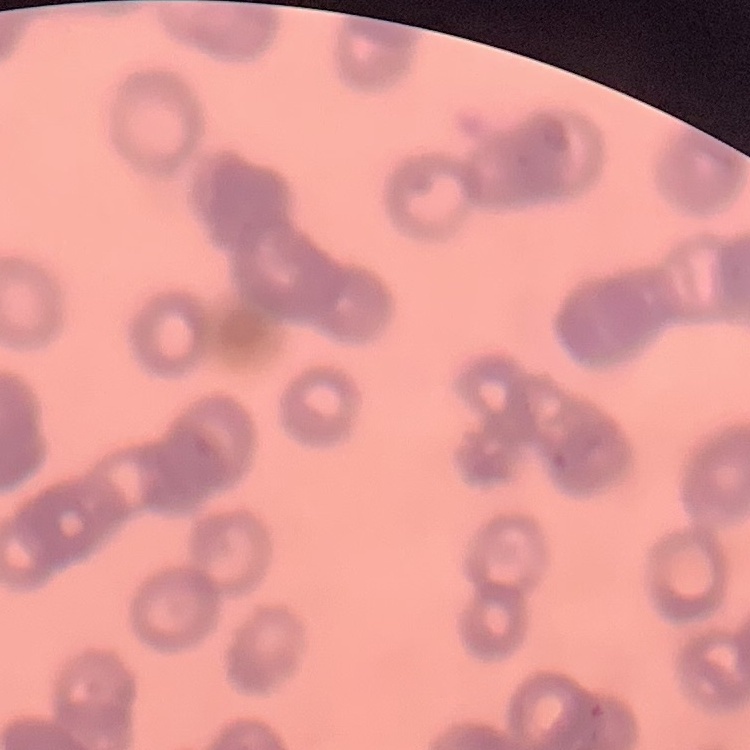

The erythrocytes exhibit rouleaux formation. Thin blood film. One tile cut from a larger photomicrograph. Field's or Giemsa stain.